Locate every Plasmodium vivax-infected red blood cell.
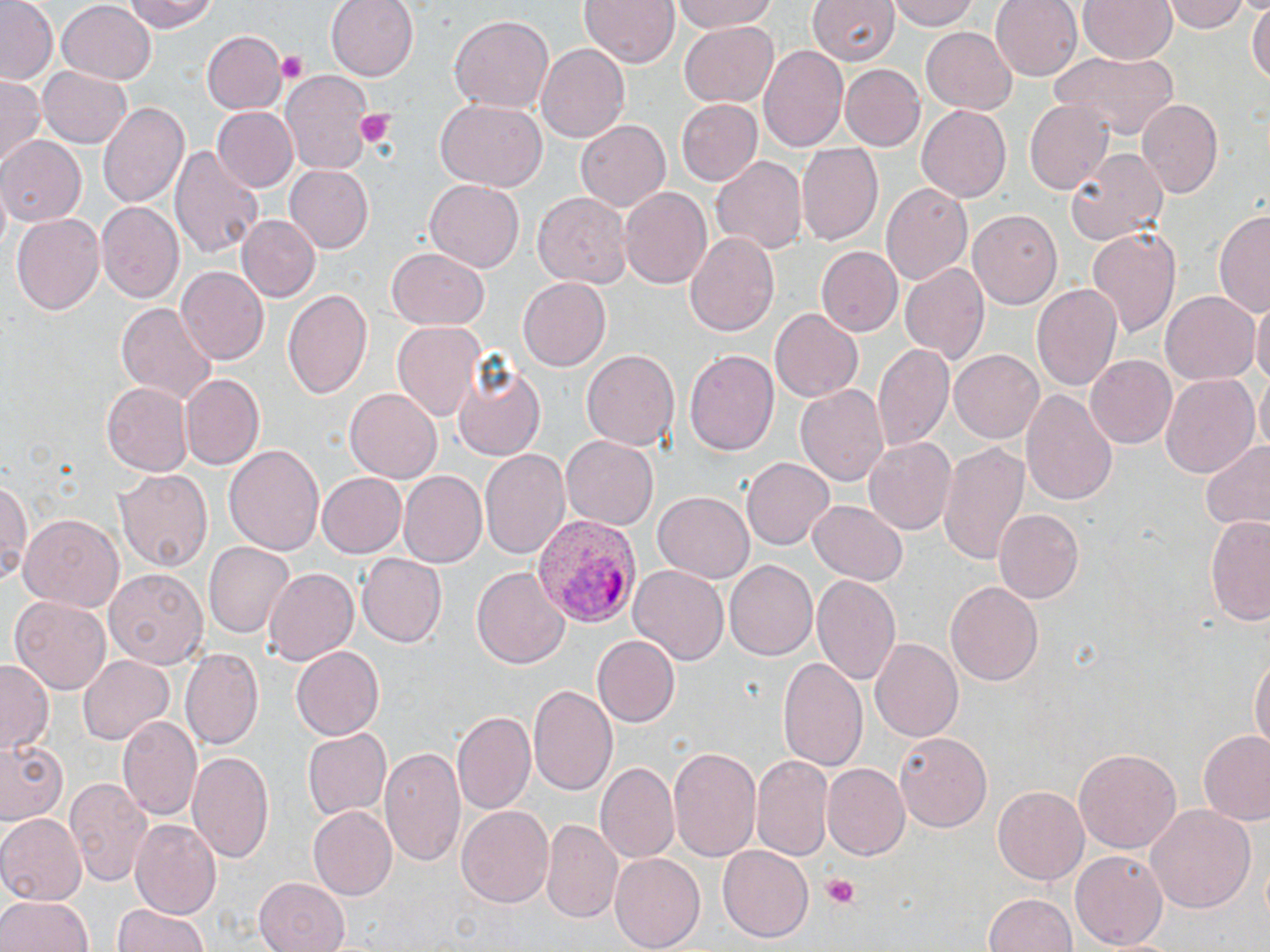
Approximate bounding boxes as (x1,y1)-(x2,y2) corner pairs in pixels.
Plasmodium vivax-infected red blood cells: (529,514)-(641,629).

{
  "slide_level_diagnosis": "Plasmodium vivax",
  "field_of_view": "single",
  "preparation": "thin blood film",
  "modality": "optical microscopy",
  "stain": "May-Grünwald-Giemsa",
  "image_size": "1270×952 pixels",
  "uninfected_red_blood_cell_locations": "approximate bounding boxes as (x1,y1)-(x2,y2) corner pairs in pixels: (1,0)-(56,84), (122,0)-(220,33), (326,0)-(419,81), (578,0)-(677,67), (668,0)-(783,33), (805,0)-(900,65), (886,0)-(983,31), (991,0)-(1082,81), (1079,0)-(1176,64), (1164,0)-(1252,35), (1248,1)-(1269,92), (56,3)-(154,84), (448,13)-(555,113), (677,20)-(779,110), (919,26)-(1016,116), (202,31)-(285,113), (535,43)-(628,144), (759,46)-(848,152), (1052,49)-(1180,141), (838,63)-(925,152), (38,66)-(134,149), (281,70)-(375,176), (0,75)-(42,170), (675,98)-(763,186), (1137,98)-(1224,201), (98,99)-(190,211), (436,100)-(546,190), (1023,100)-(1113,195), (915,105)-(1010,205), (214,106)-(300,193), (576,119)-(672,213), (0,137)-(85,227), (171,143)-(265,261), (798,144)-(883,246), (1065,148)-(1168,248), (711,156)-(807,254), (283,165)-(371,252), (424,178)-(524,272), (881,181)-(972,284), (620,185)-(713,287), (533,191)-(629,286), (98,203)-(185,303), (1217,206)-(1270,320), (969,208)-(1065,308), (10,211)-(105,318), (236,215)-(319,302), (1086,225)-(1181,340), (683,229)-(779,338), (818,247)-(901,338), (387,248)-(488,329), (899,263)-(989,366), (176,266)-(269,364), (516,277)-(611,371), (1031,282)-(1122,394), (281,288)-(373,404), (1161,290)-(1259,384), (1250,297)-(1270,395), (116,300)-(217,404), (769,308)-(864,401), (390,321)-(484,424), (872,340)-(955,449), (581,349)-(679,451), (684,349)-(780,457), (950,350)-(1043,442), (452,355)-(546,465), (1086,355)-(1176,449), (181,373)-(266,469), (1158,373)-(1259,481), (1254,373)-(1270,458), (103,381)-(193,476), (797,384)-(892,487), (1021,386)-(1117,505), (346,387)-(443,482), (560,434)-(659,532), (864,436)-(957,537), (935,439)-(1031,567), (1198,440)-(1270,531), (226,444)-(324,558), (480,448)-(569,562), (741,457)-(834,550), (115,467)-(212,573), (315,471)-(406,557), (398,472)-(488,567), (0,475)-(33,585), (684,477)-(833,575), (654,493)-(753,583), (808,499)-(908,585), (993,507)-(1083,603), (1205,513)-(1270,629), (18,514)-(125,611), (205,543)-(292,638), (357,552)-(447,645), (723,560)-(818,663), (630,565)-(728,666), (471,566)-(568,671), (261,567)-(358,666), (104,568)-(208,669), (813,575)-(902,685), (945,581)-(1043,687), (10,595)-(113,695), (594,637)-(679,725), (868,639)-(963,744), (292,645)-(384,740), (180,647)-(265,749), (79,653)-(172,743), (1250,653)-(1269,756), (777,656)-(868,773), (0,661)-(53,755), (527,683)-(618,798), (453,709)-(536,814), (118,714)-(203,821), (301,728)-(391,821), (894,731)-(992,834), (1199,731)-(1270,825), (0,736)-(68,826), (380,744)-(466,869), (668,744)-(762,863), (1072,746)-(1180,854), (187,748)-(276,865), (753,756)-(832,860), (598,762)-(677,862), (820,764)-(909,860), (65,777)-(153,889), (992,785)-(1089,887), (1144,800)-(1256,912), (309,805)-(397,900), (455,805)-(553,908), (0,813)-(86,903), (541,817)-(623,924), (131,820)-(222,920), (718,846)-(813,942), (1070,849)-(1168,951), (610,853)-(704,951), (252,876)-(350,952), (0,892)-(94,952), (981,893)-(1080,952), (111,903)-(215,952)",
  "platelet_locations": "approximate bounding boxes as (x1,y1)-(x2,y2) corner pairs in pixels: (276,52)-(308,81), (352,109)-(399,151), (817,873)-(862,907)",
  "magnification": "1000x"
}